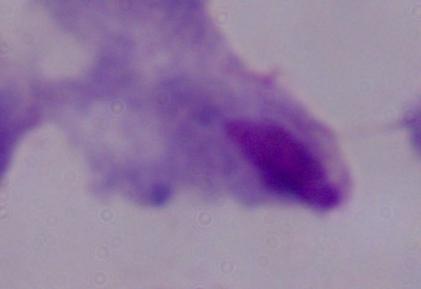

Summary:
  - Identification: trichomonad
  - Modality: photomicrograph
  - Magnification: 1000x